Locate every blood parasite and identify its species.
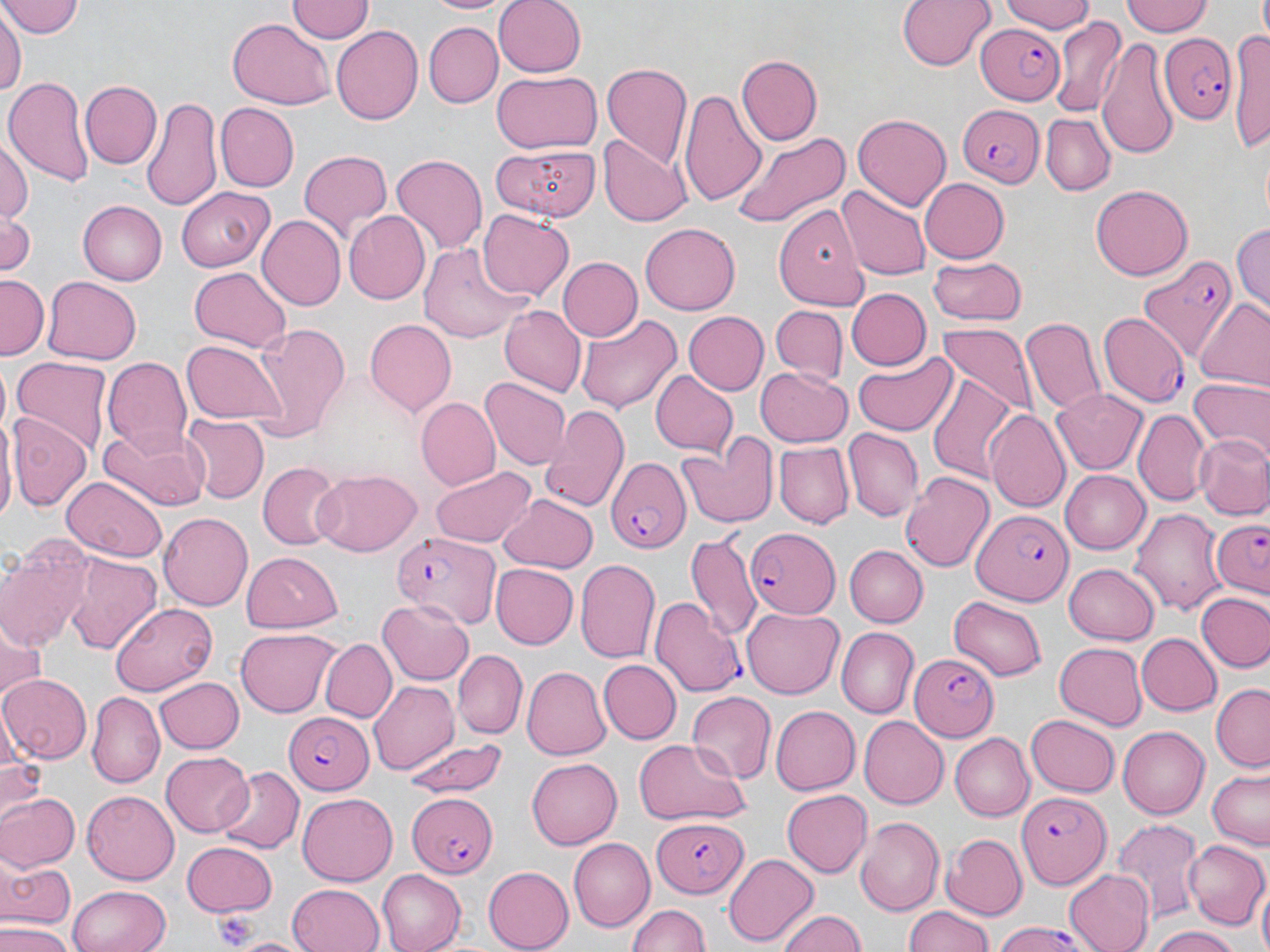
Approximate bounding boxes as (x1,y1)-(x2,y2) corner pairs in pixels.
Plasmodium falciparum-infected red blood cells: (974,25)-(1071,106), (1158,30)-(1240,121), (956,101)-(1043,185), (1137,255)-(1237,360), (1100,311)-(1190,407), (603,456)-(691,551), (969,509)-(1074,607), (1208,519)-(1269,603), (744,525)-(837,617), (390,532)-(499,627), (651,597)-(745,696), (911,656)-(1000,741), (281,712)-(372,791), (1016,792)-(1110,884), (405,793)-(497,879), (649,821)-(751,896), (989,921)-(1097,952).
No Plasmodium ovale, Plasmodium malariae, Plasmodium vivax, Babesia divergens, or Trypanosoma brucei observed.

Summary:
  - Platelet locations: (209,906)-(259,950)
  - Uninfected red blood cell locations: (4,0)-(83,39), (425,0)-(511,16), (491,0)-(586,79), (898,0)-(993,70), (1004,0)-(1098,35), (1122,0)-(1211,37), (287,2)-(373,44), (1,12)-(23,102), (228,15)-(335,107), (1051,15)-(1126,118), (1232,20)-(1270,157), (423,23)-(503,106), (329,26)-(424,126), (1098,38)-(1181,161), (737,56)-(823,143), (600,63)-(691,170), (493,71)-(600,153), (4,76)-(92,188), (78,78)-(161,167), (681,88)-(768,208), (142,96)-(223,214), (218,105)-(299,192), (853,113)-(951,209), (1041,114)-(1115,195), (733,130)-(851,231), (600,135)-(690,225), (0,138)-(30,231), (490,141)-(599,220), (297,150)-(390,246), (390,152)-(488,253), (917,178)-(1008,263), (839,185)-(931,281), (1090,185)-(1195,281), (176,187)-(275,270), (771,198)-(869,323), (77,201)-(167,285), (477,209)-(575,302), (345,212)-(430,303), (0,213)-(38,275), (258,215)-(347,310), (641,220)-(739,311), (1231,220)-(1269,314), (419,239)-(532,342), (928,256)-(1027,326), (556,257)-(641,342), (189,266)-(290,353), (0,274)-(48,361), (42,274)-(142,364), (846,289)-(933,371), (1194,299)-(1270,391), (500,306)-(585,396), (772,308)-(847,381), (575,313)-(681,413), (686,313)-(768,393), (1019,316)-(1105,417), (249,320)-(351,440), (365,320)-(456,416), (937,324)-(1037,420), (181,338)-(286,426), (853,352)-(959,439), (11,356)-(111,460), (104,358)-(194,458), (758,366)-(852,447), (650,371)-(738,455), (481,375)-(571,469), (928,375)-(1022,485), (1187,379)-(1269,463), (1052,389)-(1149,476), (417,398)-(499,490), (540,404)-(630,513), (984,408)-(1071,512), (1134,409)-(1210,507), (7,411)-(92,513), (1,415)-(17,528), (182,415)-(268,502), (99,420)-(206,510), (843,429)-(922,522), (1193,432)-(1269,521), (678,439)-(776,527), (774,442)-(854,528), (259,463)-(339,550), (430,463)-(536,548), (313,470)-(422,556), (1059,470)-(1152,554), (900,472)-(994,573), (61,478)-(166,562), (496,493)-(597,572), (1130,506)-(1229,619), (160,512)-(255,611), (685,530)-(761,643), (843,545)-(926,628), (241,551)-(343,632), (1,552)-(86,650), (63,552)-(163,653), (576,557)-(661,667), (1065,562)-(1161,645), (491,563)-(577,649), (1195,590)-(1270,675), (948,594)-(1048,681), (378,596)-(475,686), (109,602)-(216,694), (741,607)-(845,699), (0,626)-(47,707), (235,626)-(339,718), (837,628)-(918,717), (1137,632)-(1222,714), (318,636)-(396,720), (1054,642)-(1148,729), (453,649)-(526,737), (599,660)-(682,743), (521,666)-(610,761), (0,674)-(91,765), (154,676)-(243,754), (367,681)-(459,776), (1210,686)-(1270,769), (687,691)-(777,782), (88,692)-(163,785), (771,705)-(860,795), (1025,714)-(1121,797), (859,717)-(948,808), (1119,725)-(1209,819), (948,732)-(1034,821), (406,738)-(508,798), (632,740)-(751,827), (161,751)-(255,837), (0,752)-(45,815), (527,757)-(622,850), (218,765)-(301,853), (1205,769)-(1270,850), (82,790)-(179,884), (784,790)-(874,877), (0,791)-(78,872), (298,795)-(397,883), (855,815)-(944,917), (1112,819)-(1203,922), (944,835)-(1027,918), (567,837)-(654,931), (1184,840)-(1269,930), (182,841)-(278,916), (723,853)-(817,946), (0,861)-(75,929), (483,866)-(574,950), (1063,869)-(1156,952), (376,871)-(465,952), (1255,880)-(1270,952), (286,883)-(386,952), (67,884)-(172,952), (623,902)-(713,952), (902,905)-(997,952), (776,908)-(868,952), (0,922)-(72,952), (1150,926)-(1243,952), (223,936)-(311,952)
  - Slide-level diagnosis: Plasmodium falciparum
  - Modality: light microscopy
  - Image size: 1270×952 pixels
  - Magnification: 1000x
  - Preparation: thin blood smear
  - Field of view: one of a larger specimen
  - Stain: May-Grünwald-Giemsa